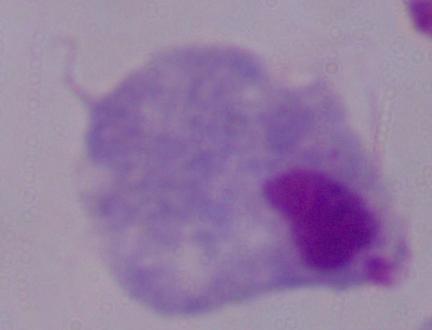 Micrograph. Captured at 1000x magnification. A trichomonad is seen.